Name the blood parasite species.
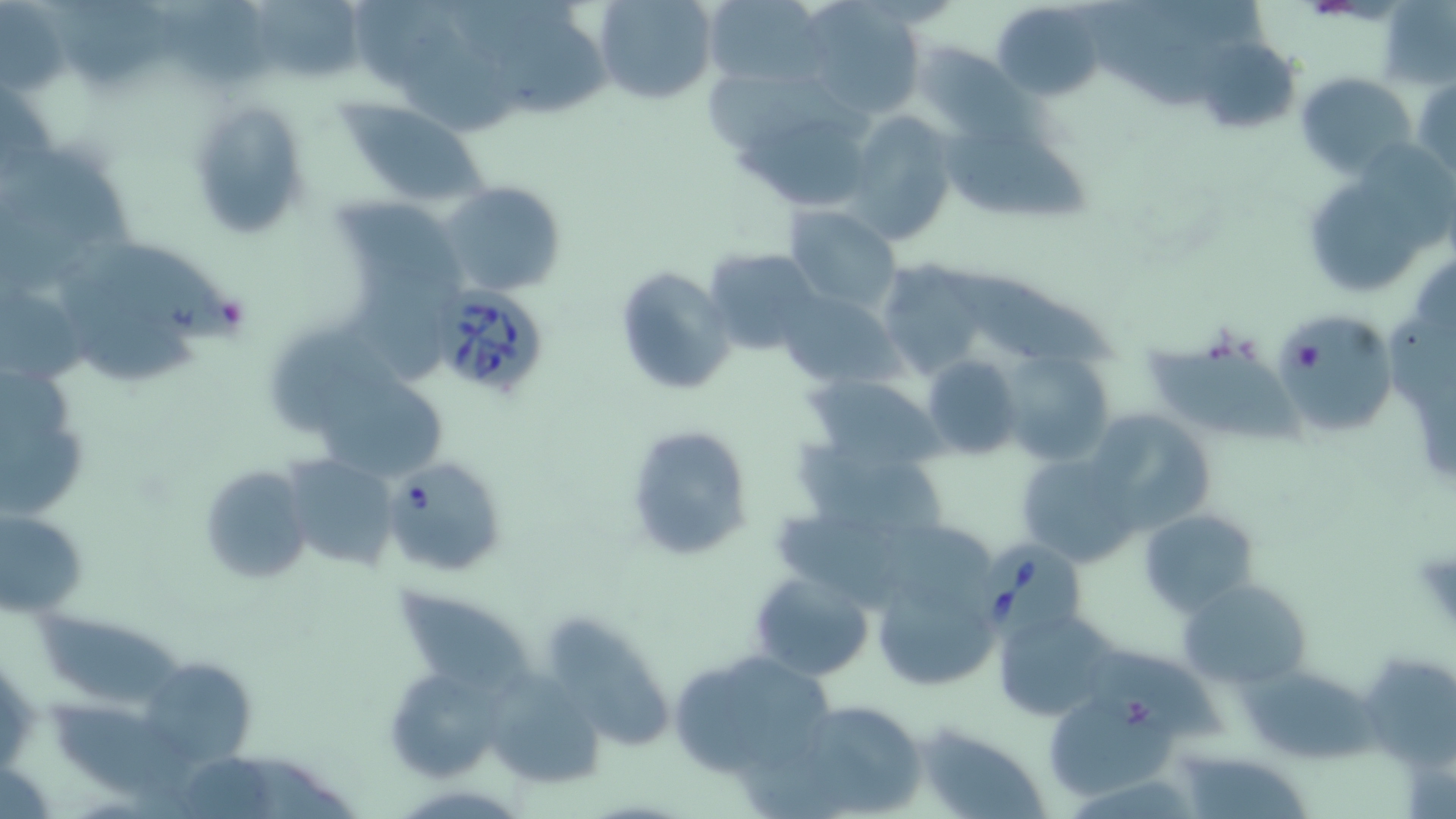

Babesia divergens.

Approximate bounding boxes as [x1, y1, x2, y2] in pixels. Babesia divergens-infected red blood cell locations: [436, 288, 550, 399], [381, 457, 508, 577], [970, 539, 1087, 642]. Uninfected red blood cell locations: [594, 0, 716, 104], [701, 0, 830, 90], [992, 0, 1105, 101], [162, 3, 290, 93], [799, 3, 922, 119], [60, 5, 175, 89], [255, 6, 379, 83], [495, 15, 612, 119], [398, 34, 519, 139], [1197, 38, 1300, 136], [915, 42, 1023, 143], [1297, 72, 1416, 179], [1414, 75, 1456, 180], [188, 98, 312, 239], [340, 102, 488, 203], [843, 110, 954, 246], [732, 117, 871, 206], [932, 128, 1101, 224], [9, 147, 146, 249], [441, 180, 568, 299], [1311, 184, 1426, 297], [340, 200, 473, 291], [782, 205, 903, 314], [78, 237, 250, 348], [703, 248, 824, 356], [876, 259, 989, 379], [615, 265, 738, 396], [944, 271, 1122, 374], [778, 290, 902, 389], [63, 302, 202, 390], [1272, 310, 1398, 437], [276, 324, 418, 438], [1145, 335, 1302, 443], [1001, 352, 1116, 467], [921, 356, 1022, 458], [0, 363, 92, 524], [315, 373, 447, 483], [803, 374, 948, 474], [1086, 408, 1215, 532], [624, 423, 754, 562], [797, 444, 950, 539], [1016, 453, 1140, 565], [282, 454, 402, 571], [197, 464, 316, 585], [0, 506, 88, 618], [1138, 509, 1258, 615], [1409, 543, 1456, 635], [749, 571, 875, 680], [1179, 576, 1314, 693], [396, 583, 531, 706], [880, 588, 992, 682], [993, 607, 1120, 720], [39, 610, 189, 710], [550, 612, 671, 749], [1079, 647, 1228, 742], [669, 649, 835, 779], [1362, 655, 1456, 770], [1238, 662, 1375, 763], [150, 665, 258, 763], [479, 668, 605, 785], [387, 676, 501, 782], [1046, 695, 1181, 798], [781, 698, 928, 817], [48, 700, 206, 807], [920, 724, 1049, 818], [1188, 756, 1306, 819]. Platelet locations: [1292, 341, 1324, 375]. May-Grünwald-Giemsa-stained preparation. One field of a larger specimen. Thin blood smear. Image is 1456×819 pixels. 1000x magnification. Optical microscopy.